Assess for malaria.
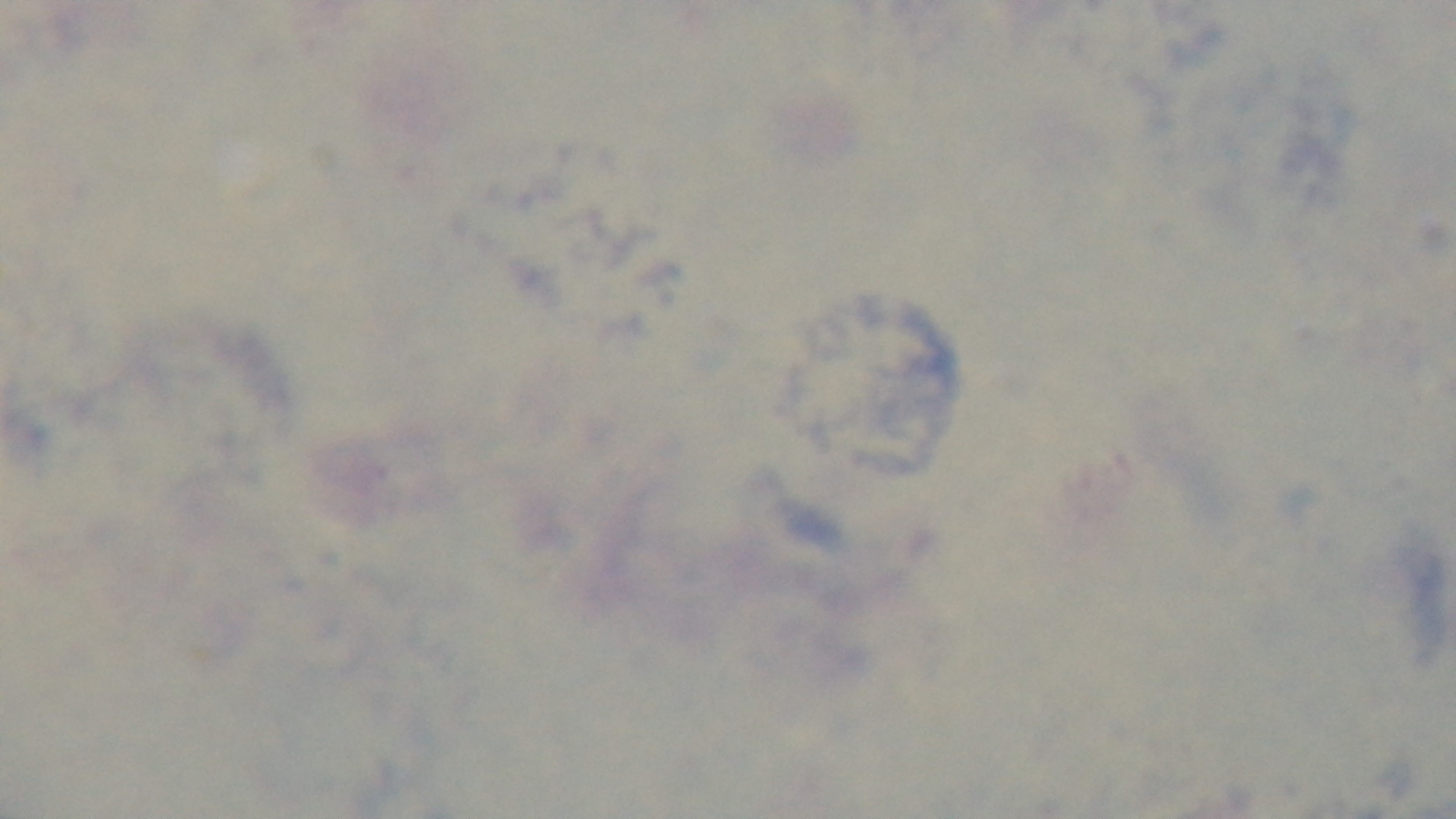

It is uninfected.

Giemsa stain. Light microscopy. Preparation: thick. Single field of view. Oil-immersion objective, 100x. Mounted 4K digital camera.